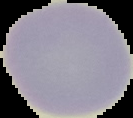

image type = segmented cell region on a black background
malaria status = uninfected
image size = 133×118 pixels
preparation = thin blood film